Name the cell type shown.
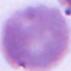

This is an erythrocyte.

modality = photomicrograph
magnification = 1000x